Report the malaria status of this cell.
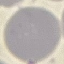
Uninfected.

Summary:
  - Preparation: thin blood smear
  - Capture: smartphone camera at the microscope eyepiece
  - Image type: automatically extracted cell patch, resized to 64 × 64 pixels
  - Stain: Giemsa